State the blood parasite species.
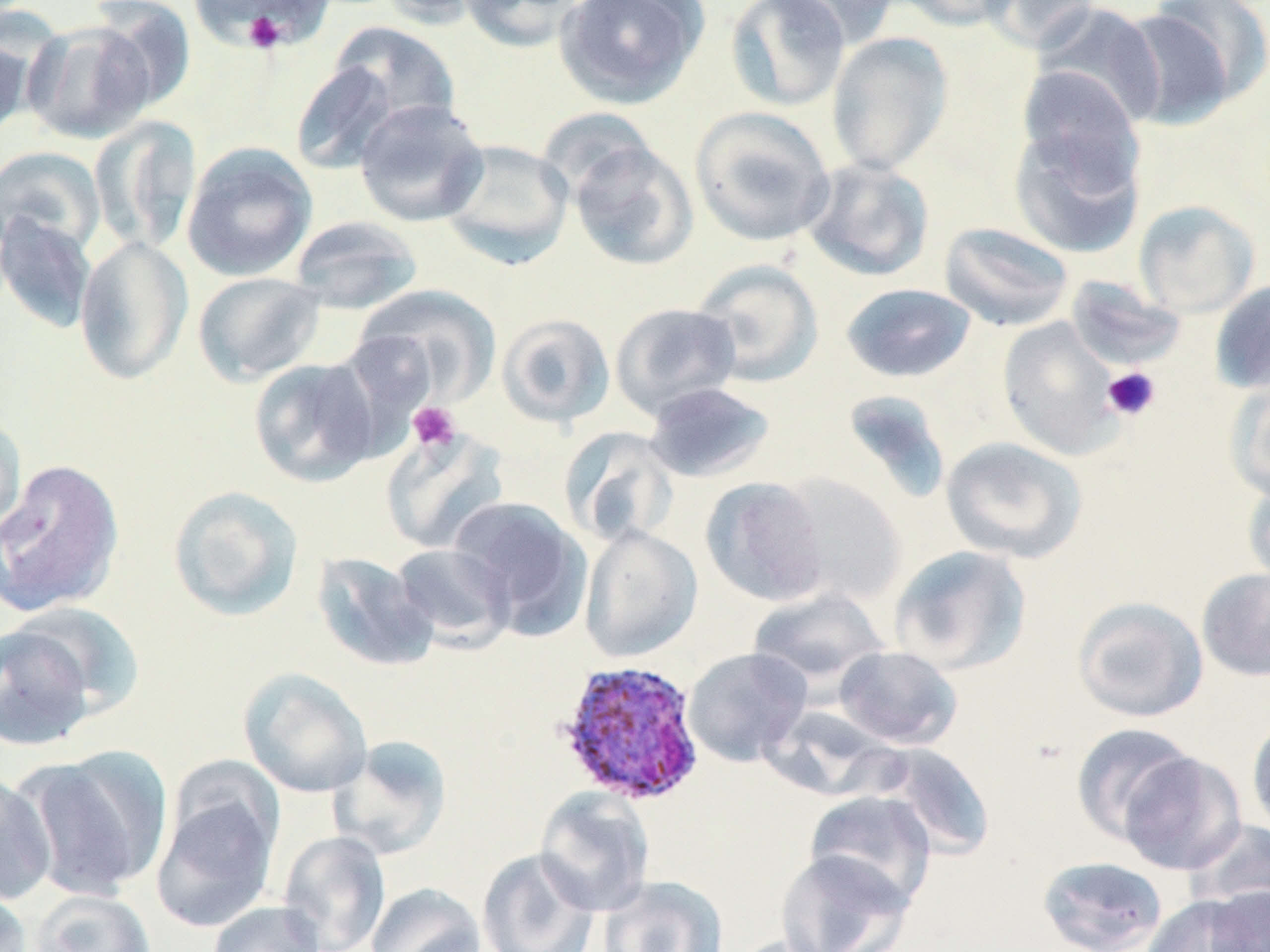
Plasmodium ovale.

{
  "image_size": "1270×952 pixels",
  "magnification": "1000x",
  "preparation": "thin blood smear",
  "platelet_locations": "approximate bounding boxes as [x1, y1, x2, y2] in pixels: [195, 1, 329, 53], [238, 7, 289, 54], [1102, 366, 1161, 421], [407, 401, 461, 452]",
  "modality": "light microscopy",
  "stain": "May-Grünwald-Giemsa",
  "uninfected_red_blood_cell_locations": "approximate bounding boxes as [x1, y1, x2, y2] in pixels: [378, 0, 494, 28], [458, 0, 586, 52], [554, 0, 708, 108], [725, 0, 850, 112], [766, 0, 900, 48], [896, 0, 1021, 31], [978, 0, 1101, 52], [89, 1, 197, 113], [190, 1, 333, 52], [1033, 2, 1166, 129], [1120, 5, 1242, 130], [22, 20, 156, 144], [329, 23, 461, 131], [0, 24, 36, 143], [826, 32, 954, 176], [290, 59, 402, 175], [1017, 67, 1144, 188], [353, 98, 489, 227], [689, 106, 836, 247], [90, 116, 202, 253], [1008, 119, 1147, 261], [438, 138, 574, 268], [567, 140, 699, 271], [182, 142, 317, 281], [0, 145, 107, 258], [800, 157, 936, 282], [1133, 200, 1260, 319], [0, 211, 97, 334], [288, 215, 424, 314], [939, 221, 1075, 332], [74, 235, 192, 386], [690, 258, 824, 387], [192, 271, 327, 386], [1066, 275, 1187, 371], [1209, 280, 1270, 394], [840, 283, 976, 383], [356, 284, 502, 408], [609, 301, 743, 420], [495, 312, 616, 428], [998, 316, 1124, 460], [248, 356, 383, 487], [1228, 378, 1270, 501], [643, 381, 777, 484], [841, 390, 952, 502], [0, 415, 27, 537], [559, 426, 680, 547], [381, 427, 510, 555], [940, 435, 1088, 563], [0, 458, 125, 617], [774, 473, 908, 606], [700, 476, 829, 606], [1242, 477, 1270, 591], [167, 485, 305, 621], [450, 496, 592, 638], [579, 523, 702, 662], [391, 543, 515, 649], [888, 545, 1032, 675], [311, 551, 439, 672], [1196, 566, 1270, 682], [747, 588, 889, 689], [1071, 596, 1209, 723], [7, 602, 145, 721], [0, 622, 98, 752], [833, 645, 963, 749], [683, 647, 812, 767], [239, 667, 372, 798], [761, 705, 902, 800], [1247, 712, 1270, 837], [1071, 722, 1197, 844], [328, 735, 452, 860], [875, 743, 997, 860], [21, 748, 172, 900], [1117, 751, 1247, 875], [0, 770, 57, 906], [535, 787, 655, 917], [152, 791, 279, 933], [804, 791, 937, 910], [1186, 818, 1270, 916], [278, 831, 390, 952], [477, 848, 599, 952], [774, 848, 915, 952], [1037, 855, 1169, 952], [598, 875, 729, 952], [365, 883, 486, 952], [0, 885, 33, 952], [1203, 885, 1270, 952], [30, 889, 156, 952], [1141, 894, 1258, 952], [207, 900, 326, 952]",
  "plasmodium_ovale_infected_red_blood_cell_locations": "approximate bounding boxes as [x1, y1, x2, y2] in pixels: [554, 658, 706, 806]",
  "field_of_view": "one of a larger specimen"
}